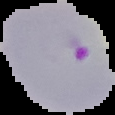 From a thin blood film. Cell region segmented out of the field of view; the surrounding area is masked to black. Malaria status: parasitized. Image is 115×115 pixels.